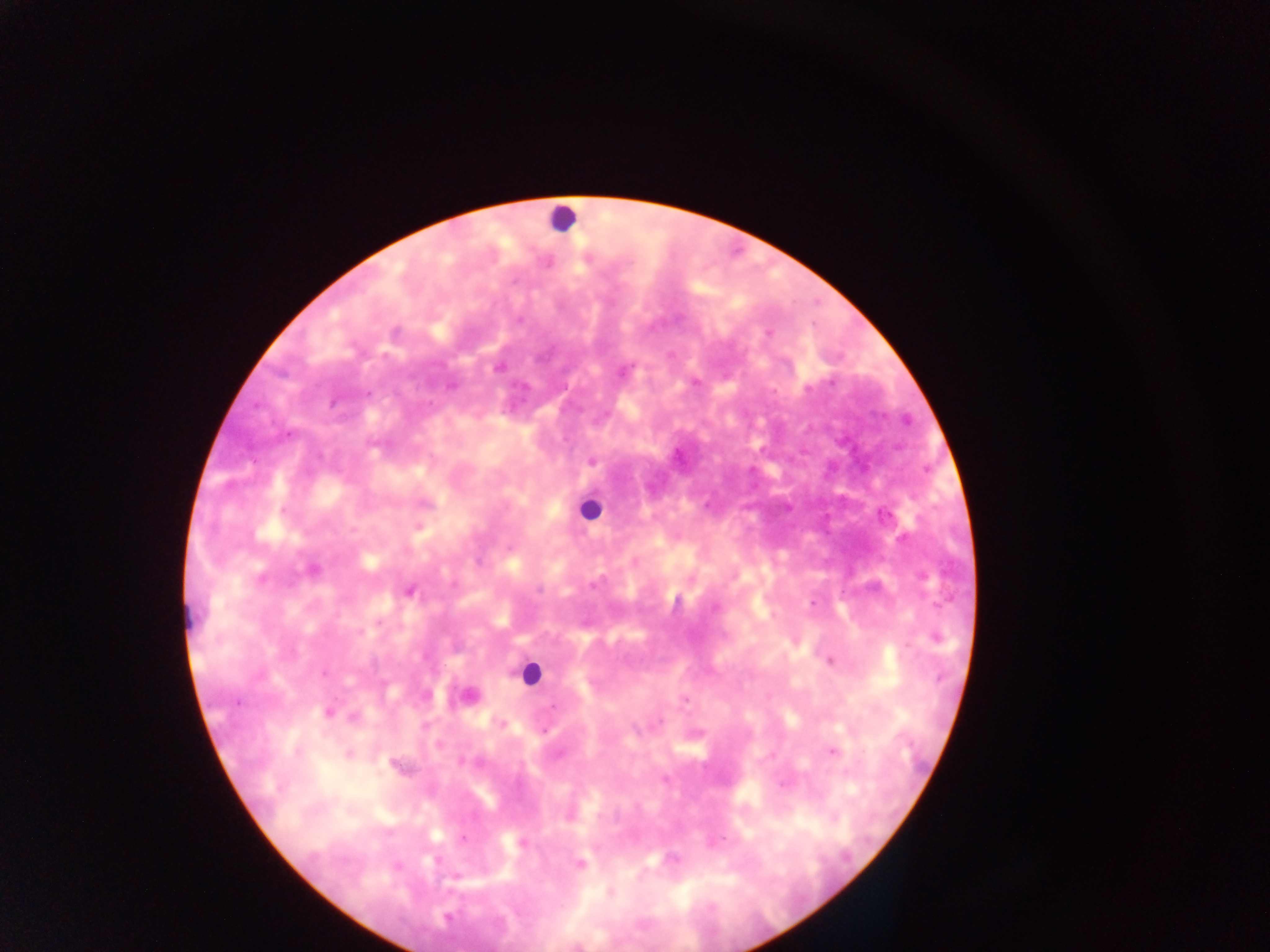

Approximate centers as x y in pixels.
Summary:
  - Leukocyte locations: 561 217; 589 508; 191 613; 529 673; 463 695
  - Plasmodium parasite locations: 768 333; 498 368; 621 372; 695 381; 450 386; 808 389; 592 462; 313 570; 260 579; 594 585; 539 590; 410 591; 813 603; 714 609; 936 638; 832 661; 324 674; 684 699; 237 703; 555 706; 329 712; 354 717; 543 731; 833 751; 297 753; 348 754; 399 766; 665 779; 462 840; 522 842; 580 864
  - Capture: mobile-phone photograph through a microscope
  - Image size: 1270×952 pixels
  - Country: Ghana
  - Field of view: single
  - Preparation: thick blood film